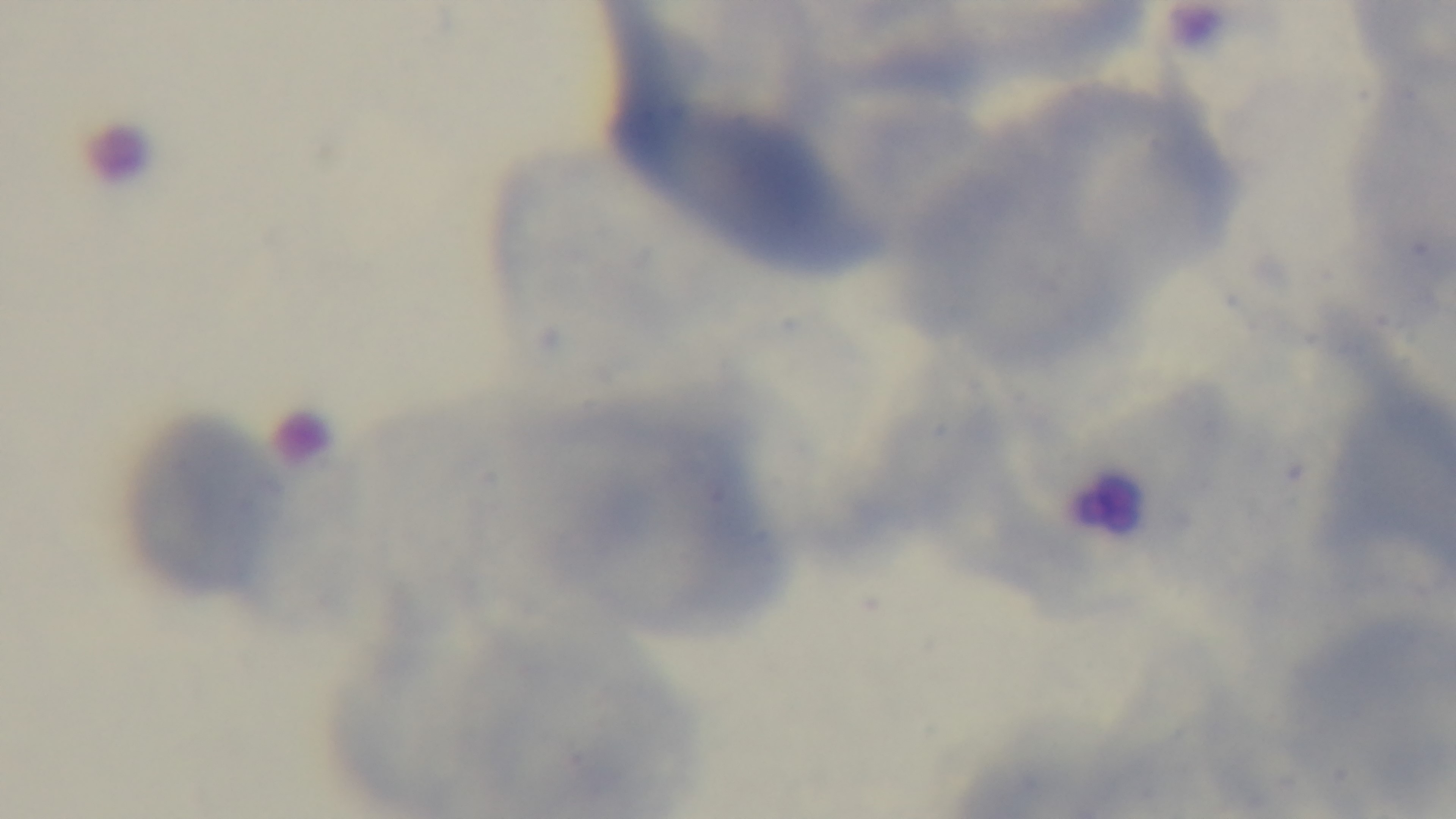

field_of_view: one from the slide
stain: Giemsa
capture: mounted 4K digital camera
modality: light microscopy
preparation: thin
objective: 100x oil immersion
malaria_status: uninfected